Report the malaria status.
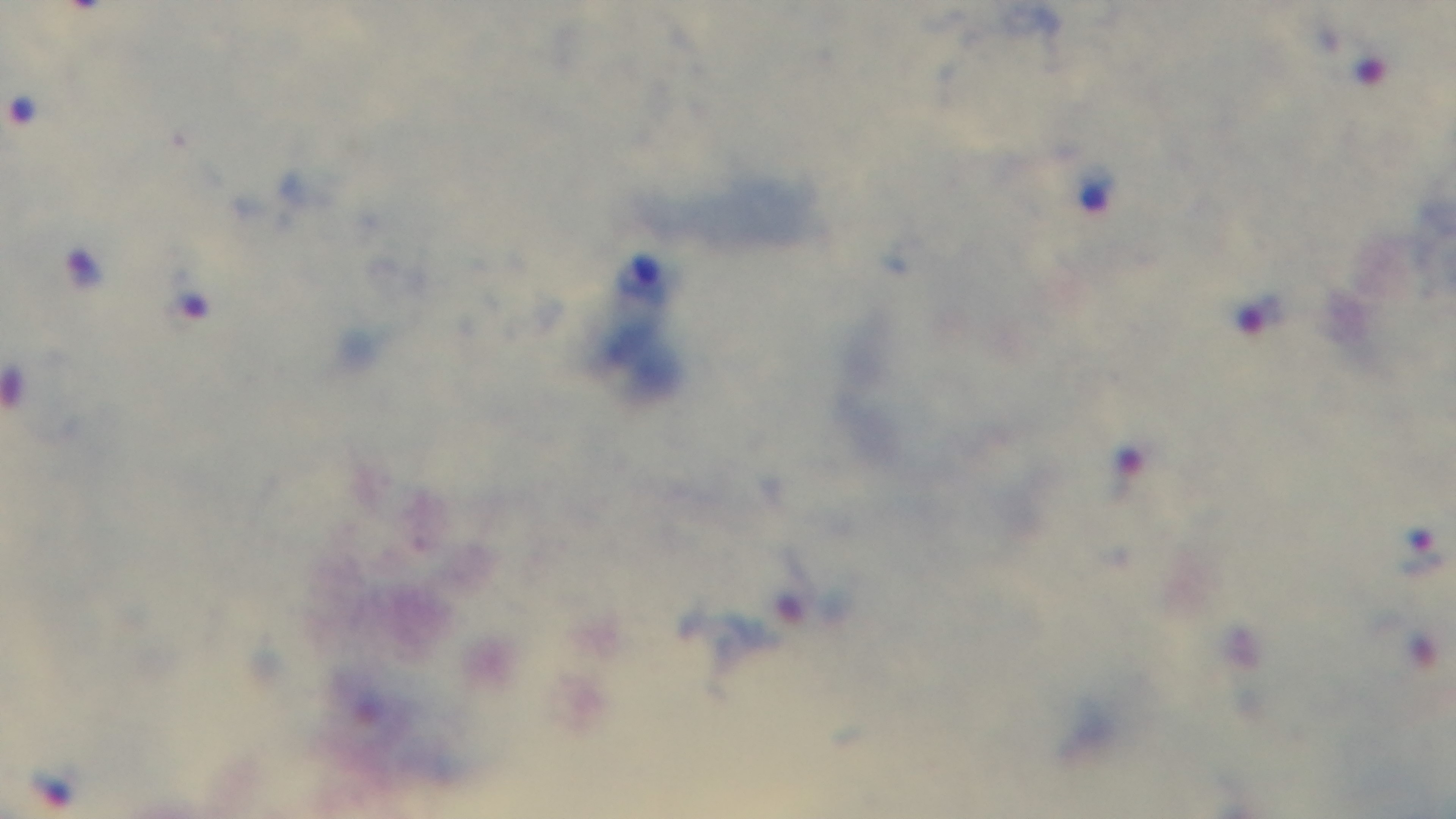

Infected.

100x oil-immersion objective. Single field of view. Light microscopy. Giemsa-stained. Preparation: thick blood film. Captured with a mounted 4K digital camera.